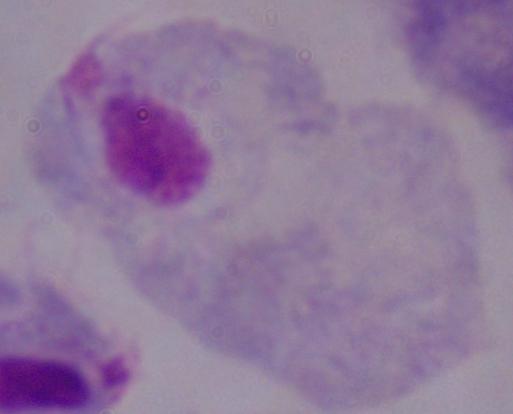
modality = photomicrograph
magnification = 1000x
identification = trichomonad